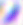 Toxoplasma gondii is shown. Micrograph. 400x magnification.